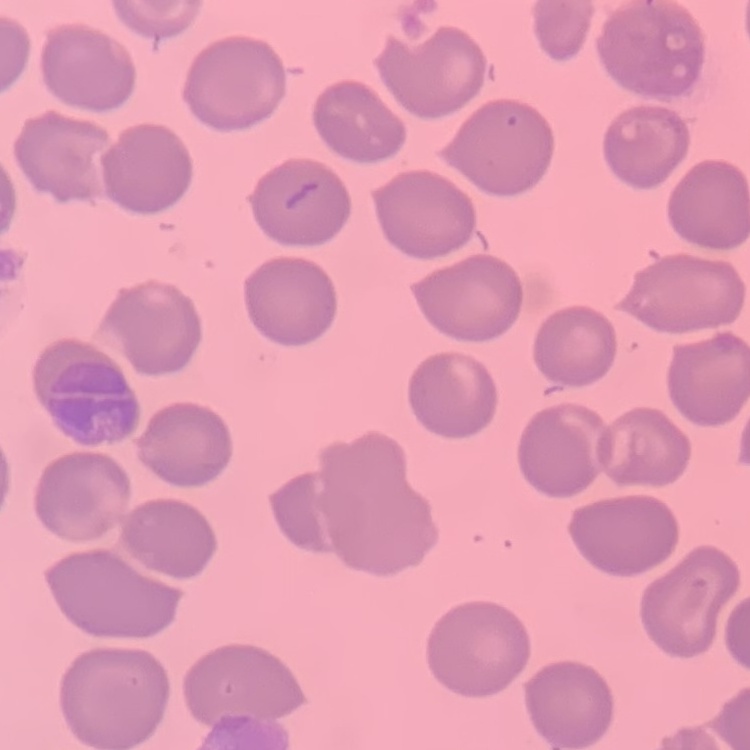 The red blood cells show no rouleaux formation. Thin blood film. Stained with either Field's or Giemsa. Square crop of a larger photomicrograph.